Locate and identify every blood parasite.
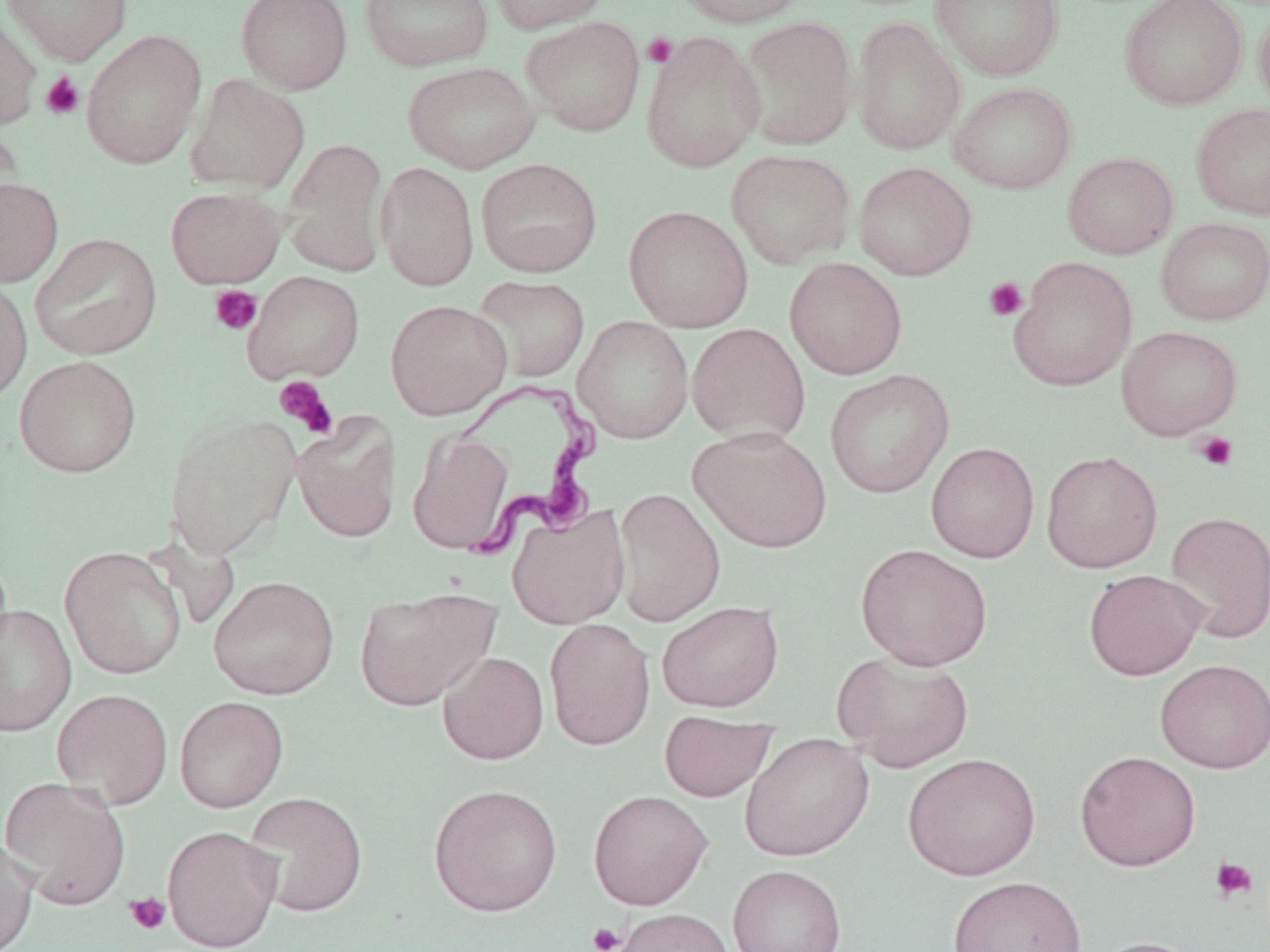
Approximate bounding boxes as (x1,y1)-(x2,y2) corner pairs in pixels.
Trypanosoma brucei: (443,380)-(602,561).
No Plasmodium falciparum, Plasmodium ovale, Plasmodium malariae, Plasmodium vivax, or Babesia divergens observed.

Summary:
  - Platelet locations: (642,32)-(678,68), (40,72)-(85,120), (244,271)-(364,395), (983,277)-(1028,322), (209,285)-(262,335), (275,377)-(338,439), (1193,431)-(1239,472), (1210,857)-(1258,903), (124,891)-(171,936), (587,922)-(626,952)
  - Uninfected red blood cell locations: (1,0)-(132,65), (235,0)-(353,94), (359,0)-(494,72), (484,0)-(613,35), (671,0)-(809,28), (930,0)-(1063,81), (1119,0)-(1247,110), (1253,1)-(1270,119), (0,8)-(42,130), (521,16)-(646,137), (737,16)-(857,151), (850,17)-(965,155), (80,29)-(207,169), (640,31)-(765,173), (402,60)-(540,173), (185,74)-(310,194), (948,82)-(1077,194), (1190,102)-(1270,221), (0,122)-(24,228), (281,138)-(389,277), (725,149)-(856,269), (1062,152)-(1179,259), (476,157)-(603,277), (375,161)-(479,291), (853,162)-(978,280), (0,177)-(64,288), (165,186)-(287,288), (623,205)-(754,333), (1155,217)-(1270,325), (29,232)-(163,361), (784,257)-(907,380), (1008,257)-(1138,392), (244,270)-(365,384), (472,275)-(590,382), (0,276)-(33,404), (385,299)-(512,419), (573,315)-(694,444), (686,323)-(810,446), (1116,325)-(1242,440), (14,355)-(143,478), (825,369)-(954,498), (164,411)-(300,560), (291,412)-(403,544), (689,425)-(832,553), (408,430)-(515,554), (926,442)-(1040,563), (1041,449)-(1163,573), (613,487)-(726,627), (506,503)-(631,630), (1164,510)-(1270,645), (855,543)-(993,671), (59,546)-(187,680), (1083,568)-(1207,681), (208,575)-(339,700), (353,585)-(501,711), (657,601)-(785,712), (0,603)-(78,737), (544,617)-(656,751), (833,650)-(974,773), (438,651)-(549,765), (1155,658)-(1270,773), (51,688)-(174,810), (174,696)-(289,812), (659,710)-(776,802), (740,732)-(874,862), (1074,750)-(1201,872), (903,752)-(1042,881), (0,776)-(132,910), (428,784)-(563,916), (588,790)-(713,910), (243,791)-(368,917), (162,825)-(283,951), (0,836)-(39,952), (728,864)-(847,952), (947,875)-(1086,952), (612,907)-(736,952), (1087,936)-(1209,952)
  - Slide-level diagnosis: Trypanosoma brucei
  - Stain: May-Grünwald-Giemsa
  - Preparation: thin blood smear
  - Modality: optical microscopy
  - Magnification: 1000x
  - Image size: 1270×952 pixels
  - Field of view: single